Describe the morphology of the erythrocytes.
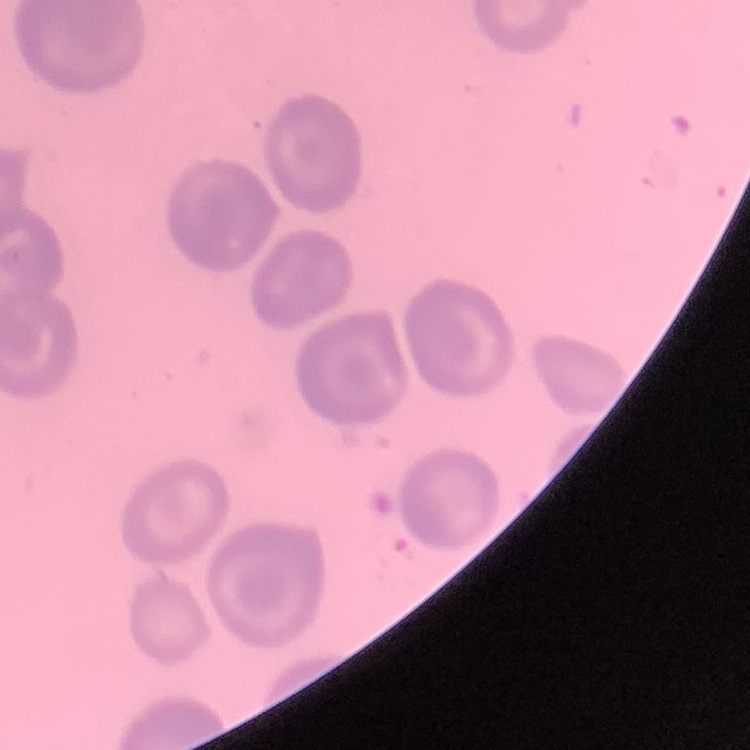

They show no rouleaux formation.

preparation = thin blood film
stain = Field's or Giemsa
image type = one tile cut from a larger photomicrograph